Point out each malaria parasite.
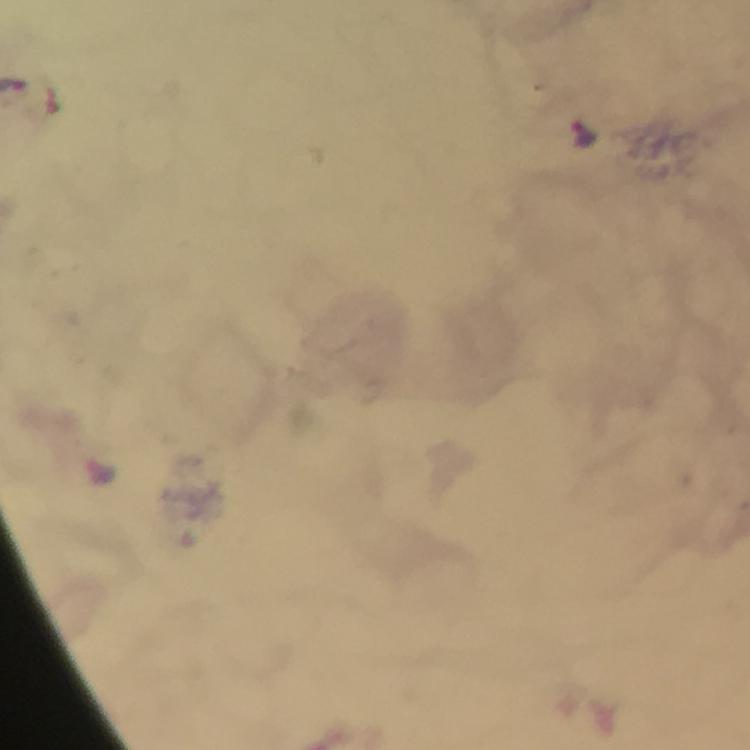

Approximate centers as [x, y] in pixels.
Malaria parasites: [584, 134], [101, 472].

Summary:
  - Cropped from: one field of view
  - Magnification: 100x
  - Immersion oil: applied
  - Image size: 750×750 pixels
  - Stain: Giemsa
  - Capture: smartphone camera through the microscope
  - Preparation: thick blood smear
  - Context: from a malaria diagnostic workup